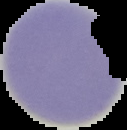 The area outside the segmented cell region is set to black. From a thin blood smear. Image is 127×130 pixels. Malaria status: uninfected.